Name the cell type shown.
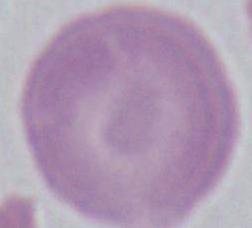
An erythrocyte.

Summary:
  - Magnification: 1000x
  - Modality: photomicrograph